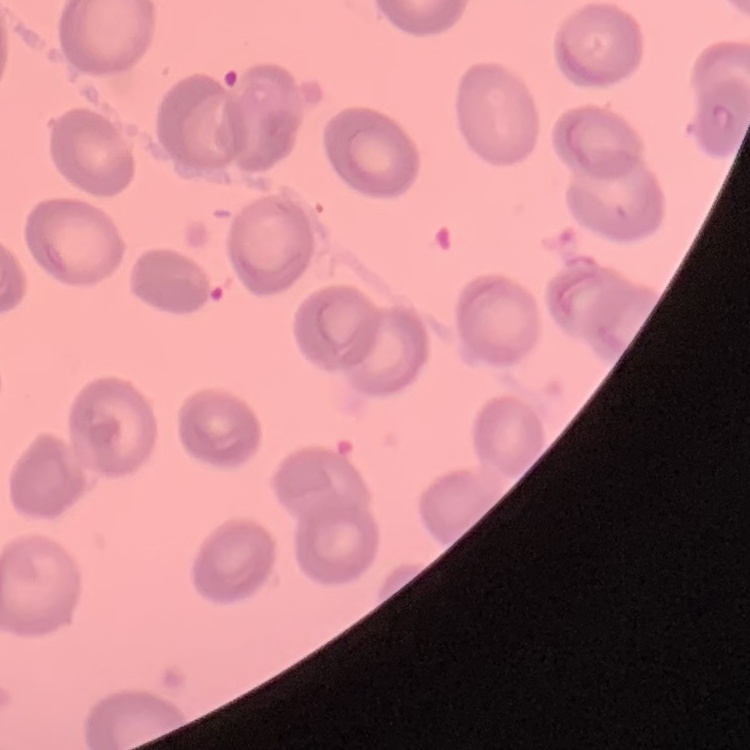

{
  "erythrocyte_morphology": "no rouleaux formation",
  "stain": "Field's or Giemsa",
  "image_type": "square crop of a larger photomicrograph",
  "preparation": "thin blood smear"
}